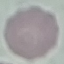

Result: no malaria parasites detected. Photographed with a smartphone camera at the microscope eyepiece. Giemsa-stained preparation. Thin smear of blood. Automatically extracted cell patch, resized to 64 × 64 pixels.